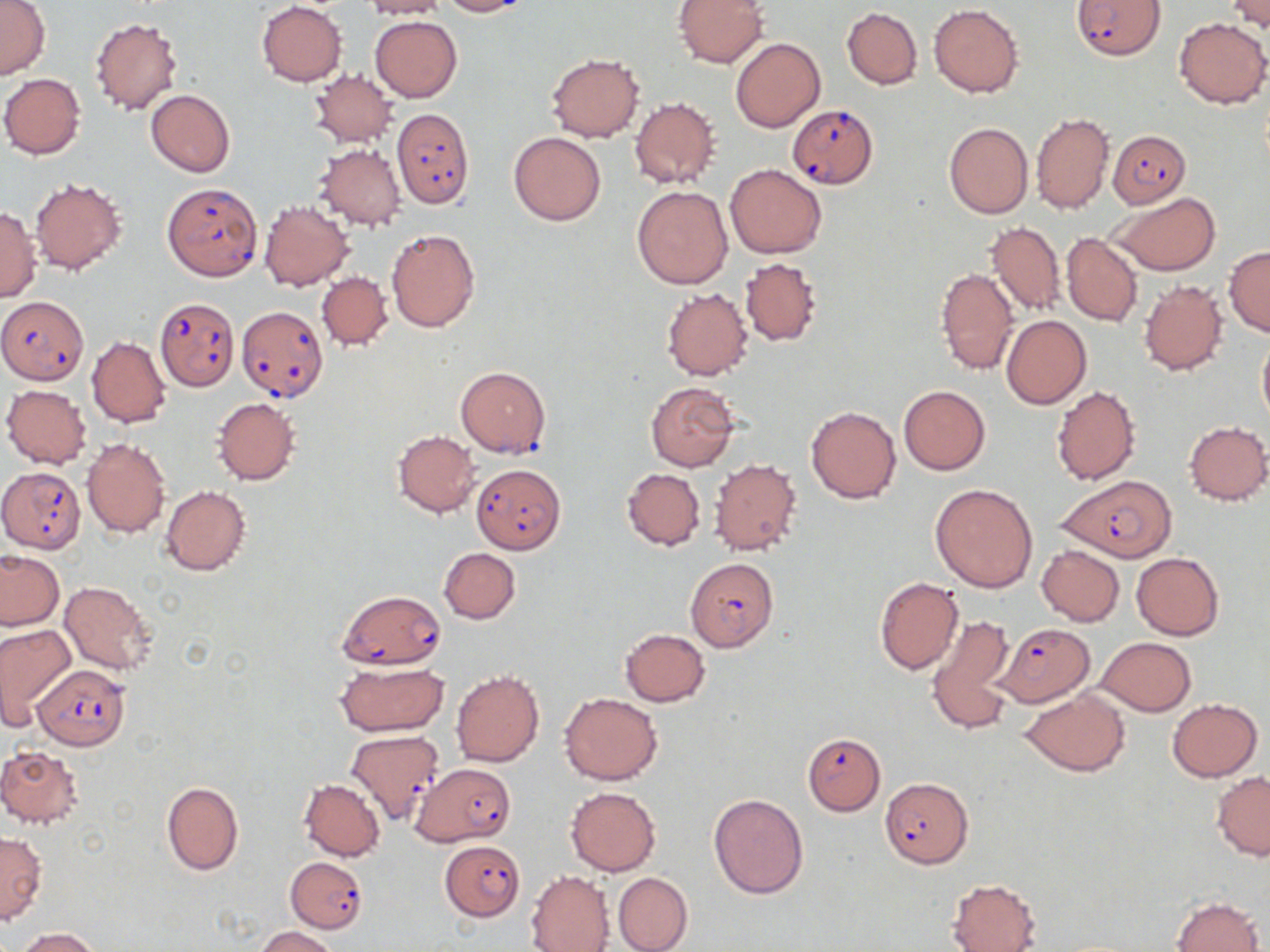
Summary:
  - Coordinate format: approximate bounding boxes as (x1,y1)-(x2,y2) corner pairs in pixels
  - Uninfected red blood cell locations: (359,0)-(450,19), (436,0)-(531,16), (0,1)-(49,79), (673,1)-(770,67), (257,2)-(347,86), (1227,3)-(1270,34), (929,4)-(1024,97), (842,6)-(923,89), (370,16)-(462,102), (89,17)-(183,115), (1174,19)-(1270,107), (731,37)-(826,132), (548,53)-(644,142), (310,70)-(397,147), (1,73)-(86,159), (146,89)-(235,176), (629,97)-(718,189), (1031,113)-(1115,215), (943,122)-(1033,219), (509,132)-(607,225), (314,143)-(406,231), (726,164)-(825,258), (30,177)-(126,274), (632,185)-(733,289), (1109,192)-(1220,275), (259,200)-(353,291), (0,207)-(40,302), (984,221)-(1066,316), (385,227)-(481,334), (1061,232)-(1143,327), (1224,245)-(1270,336), (740,257)-(821,346), (936,268)-(1018,375), (316,272)-(393,351), (1138,279)-(1228,375), (661,287)-(751,380), (1002,315)-(1091,409), (1257,334)-(1270,428), (87,336)-(171,427), (645,380)-(740,472), (2,385)-(92,469), (899,385)-(990,475), (1051,386)-(1141,486), (213,398)-(300,485), (805,405)-(901,504), (1183,420)-(1269,505), (392,430)-(481,517), (81,438)-(171,537), (709,458)-(802,557), (622,469)-(705,550), (930,483)-(1039,592), (161,485)-(251,576), (1037,545)-(1124,626), (438,547)-(520,624), (0,551)-(64,630), (1132,553)-(1225,640), (874,576)-(963,675), (59,580)-(158,675), (894,601)-(998,709), (927,615)-(1016,731), (0,623)-(75,720), (619,628)-(711,706), (1097,637)-(1196,716), (333,661)-(448,736), (451,670)-(544,768), (559,691)-(663,785), (1020,691)-(1132,776), (1167,697)-(1262,781), (0,747)-(85,829), (1212,772)-(1270,859), (298,779)-(386,861), (162,781)-(243,875), (565,786)-(660,876), (708,793)-(808,898), (0,832)-(46,924), (526,870)-(615,951), (614,872)-(693,952), (947,878)-(1041,952), (1172,896)-(1263,952), (256,926)-(339,952), (16,928)-(99,951)
  - Plasmodium falciparum-infected red blood cell locations: (1072,0)-(1165,59), (787,104)-(878,188), (391,108)-(474,208), (1106,130)-(1190,208), (162,182)-(262,280), (0,294)-(88,384), (154,297)-(239,391), (237,306)-(327,402), (455,366)-(551,456), (472,463)-(566,554), (0,467)-(87,553), (1057,474)-(1177,562), (685,558)-(778,651), (338,589)-(447,669), (995,623)-(1099,707), (31,664)-(131,749), (346,729)-(444,825), (802,732)-(886,815), (411,762)-(516,846), (879,778)-(973,868), (438,840)-(525,922), (287,855)-(368,933)
  - Slide-level diagnosis: Plasmodium falciparum
  - Modality: optical microscopy
  - Stain: May-Grünwald-Giemsa
  - Image size: 1270×952 pixels
  - Field of view: one of a larger specimen
  - Preparation: thin blood film
  - Magnification: 1000x